Assess this cell for malaria.
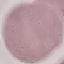

Uninfected.

Giemsa stain. Acquired by smartphone through the microscope eyepiece. Cell patch, automatically extracted from a larger field of view and resized to 64 × 64 pixels. Thin blood film.